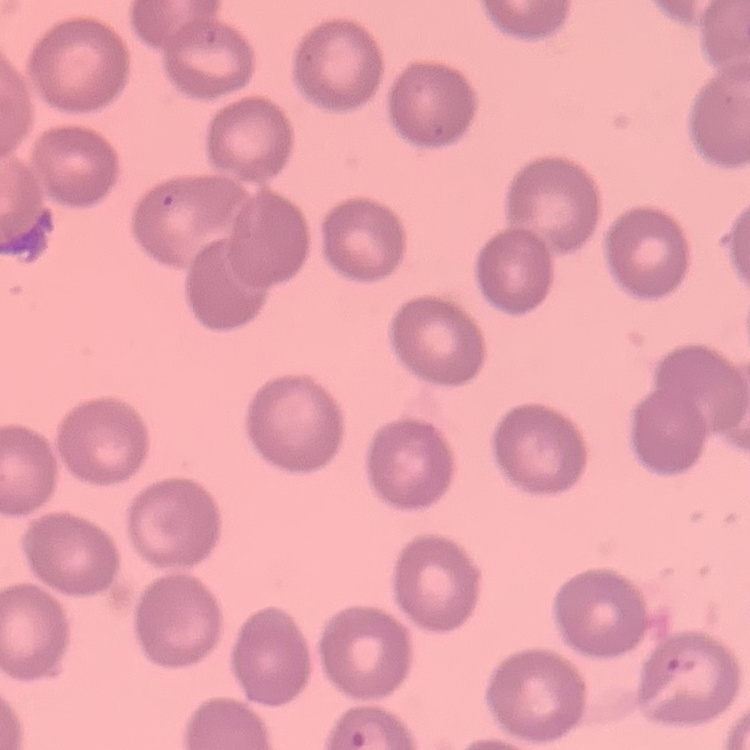
Summary:
  - Erythrocyte morphology: no rouleaux formation
  - Stain: Field's or Giemsa
  - Preparation: thin blood film
  - Image type: square crop of a larger photomicrograph